Locate every Plasmodium malariae-infected red blood cell.
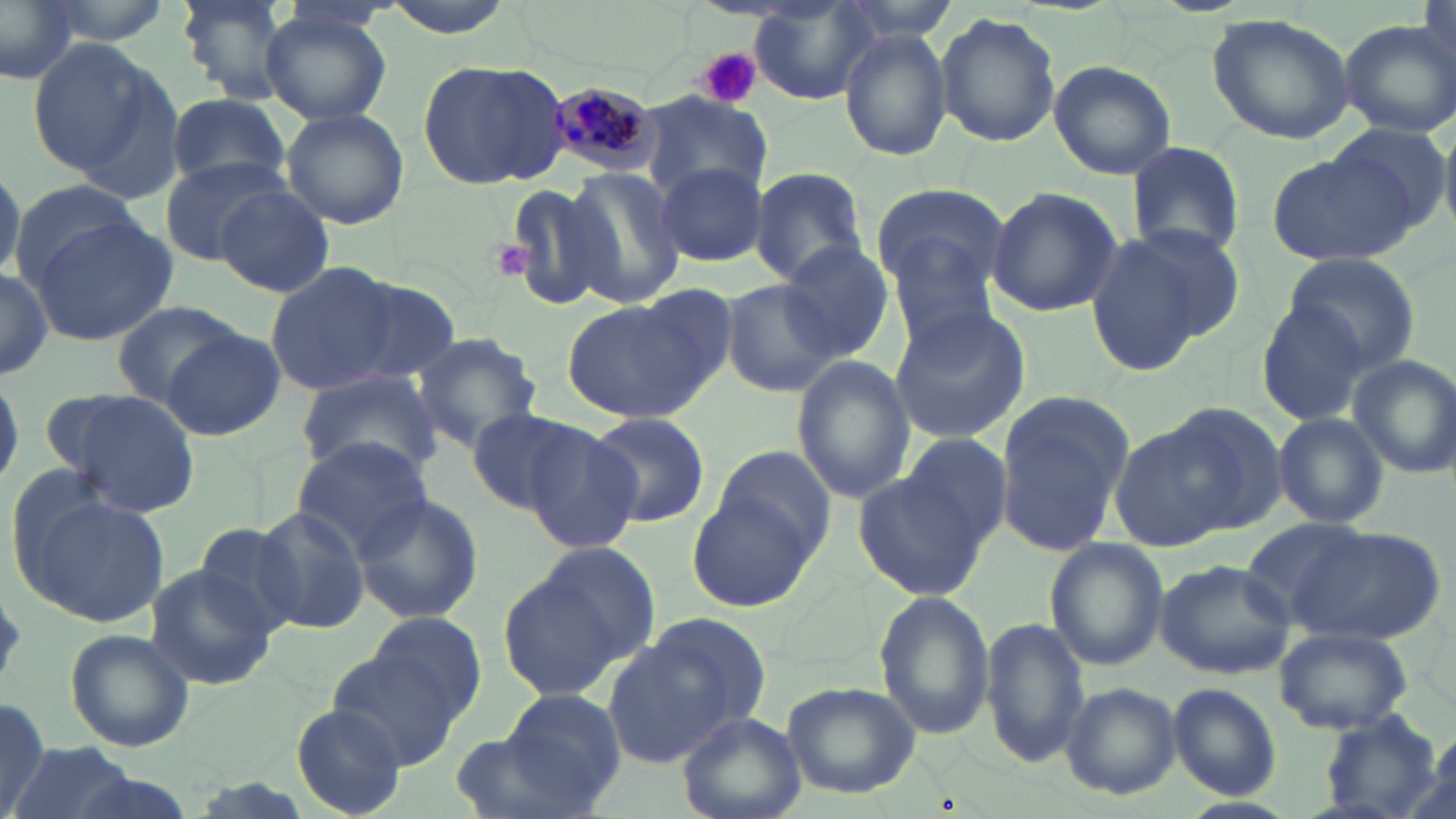

Approximate bounding boxes as [x1, y1, x2, y2] in pixels.
Plasmodium malariae-infected red blood cells: [544, 78, 664, 182].

Platelet locations: [698, 47, 762, 109], [490, 242, 540, 282]. Uninfected red blood cell locations: [0, 0, 80, 85], [174, 0, 294, 102], [750, 4, 883, 107], [260, 9, 393, 127], [937, 13, 1062, 146], [1206, 13, 1356, 143], [1340, 20, 1455, 135], [840, 28, 953, 162], [25, 37, 167, 184], [418, 59, 570, 191], [1048, 60, 1177, 179], [163, 91, 291, 195], [640, 93, 768, 200], [280, 106, 410, 230], [1313, 123, 1455, 248], [1127, 142, 1246, 260], [1266, 145, 1424, 268], [159, 157, 287, 268], [655, 159, 768, 267], [749, 165, 869, 286], [563, 166, 688, 311], [0, 167, 22, 286], [500, 179, 622, 315], [9, 180, 146, 283], [213, 182, 335, 296], [869, 186, 1011, 297], [985, 186, 1122, 318], [25, 212, 177, 348], [1115, 220, 1245, 349], [1083, 234, 1205, 376], [883, 235, 1004, 351], [777, 243, 892, 360], [1279, 251, 1421, 371], [265, 264, 396, 394], [0, 265, 55, 382], [329, 275, 461, 389], [722, 280, 836, 398], [560, 296, 725, 425], [1256, 296, 1376, 428], [111, 300, 241, 407], [888, 304, 1030, 444], [161, 327, 288, 440], [409, 332, 542, 449], [1347, 354, 1456, 478], [792, 355, 914, 505], [296, 368, 443, 481], [52, 387, 201, 516], [993, 393, 1137, 556], [1163, 401, 1288, 531], [464, 406, 591, 514], [585, 410, 711, 528], [1272, 412, 1392, 530], [524, 422, 643, 552], [1112, 425, 1240, 550], [902, 434, 1013, 546], [292, 437, 434, 556], [711, 445, 838, 560], [853, 471, 992, 602], [19, 486, 169, 630], [689, 489, 819, 612], [351, 491, 483, 624], [251, 506, 372, 634], [1238, 517, 1369, 628], [189, 521, 305, 637], [1288, 523, 1444, 643], [1044, 537, 1168, 671], [530, 540, 661, 667], [1156, 557, 1300, 679], [143, 563, 278, 691], [497, 572, 623, 699], [873, 591, 996, 741], [367, 611, 486, 722], [642, 611, 773, 740], [982, 616, 1087, 768], [1274, 626, 1413, 734], [66, 629, 195, 753], [603, 639, 732, 767], [327, 645, 465, 771], [781, 680, 921, 798], [1060, 682, 1181, 799], [1169, 684, 1282, 800], [496, 689, 627, 808], [0, 696, 50, 818], [291, 704, 411, 817], [678, 712, 806, 819], [1316, 715, 1444, 816], [449, 731, 594, 819], [8, 742, 139, 819]. Slide-level diagnosis: Plasmodium malariae. May-Grünwald-Giemsa stain. Light microscopy. Captured at 1000x magnification. Thin blood smear. One field of a larger specimen. Image is 1456×819 pixels.